Point out malaria parasites and leukocytes.
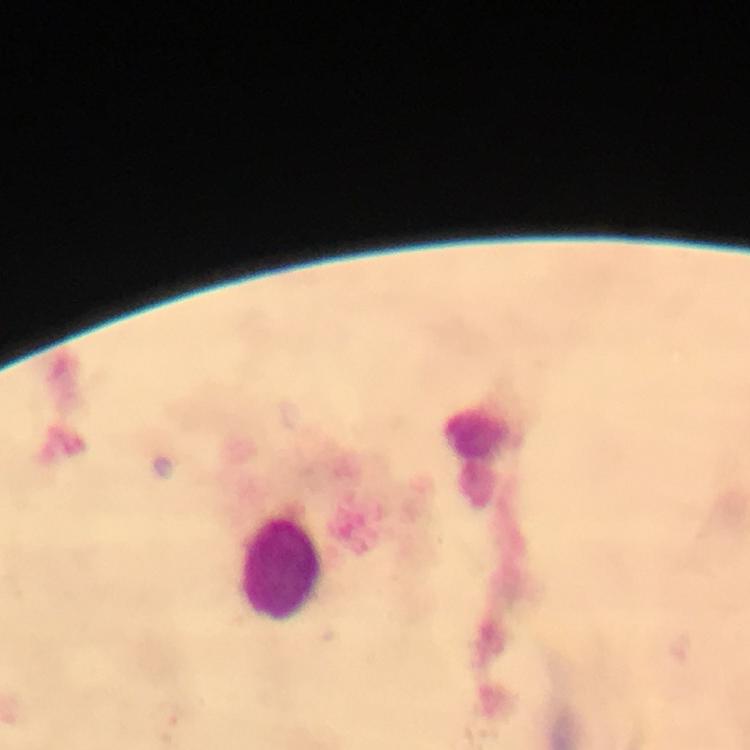

No malaria parasites detected.
Approximate object centers, in pixels from the top-left corner.
Leukocytes: (x=478, y=453), (x=281, y=571).

capture = smartphone mounted on the microscope
preparation = thick blood film
image size = 750×750 pixels
immersion oil = applied
magnification = 100x
stain = Giemsa
cropped from = one field of view
context = from a diagnostic examination for malaria